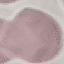
Summary:
  - Malaria status: uninfected
  - Stain: Giemsa
  - Image type: cell patch, automatically extracted from a larger field of view and resized to 64 × 64 pixels
  - Preparation: thin blood film
  - Capture: smartphone camera at the microscope eyepiece